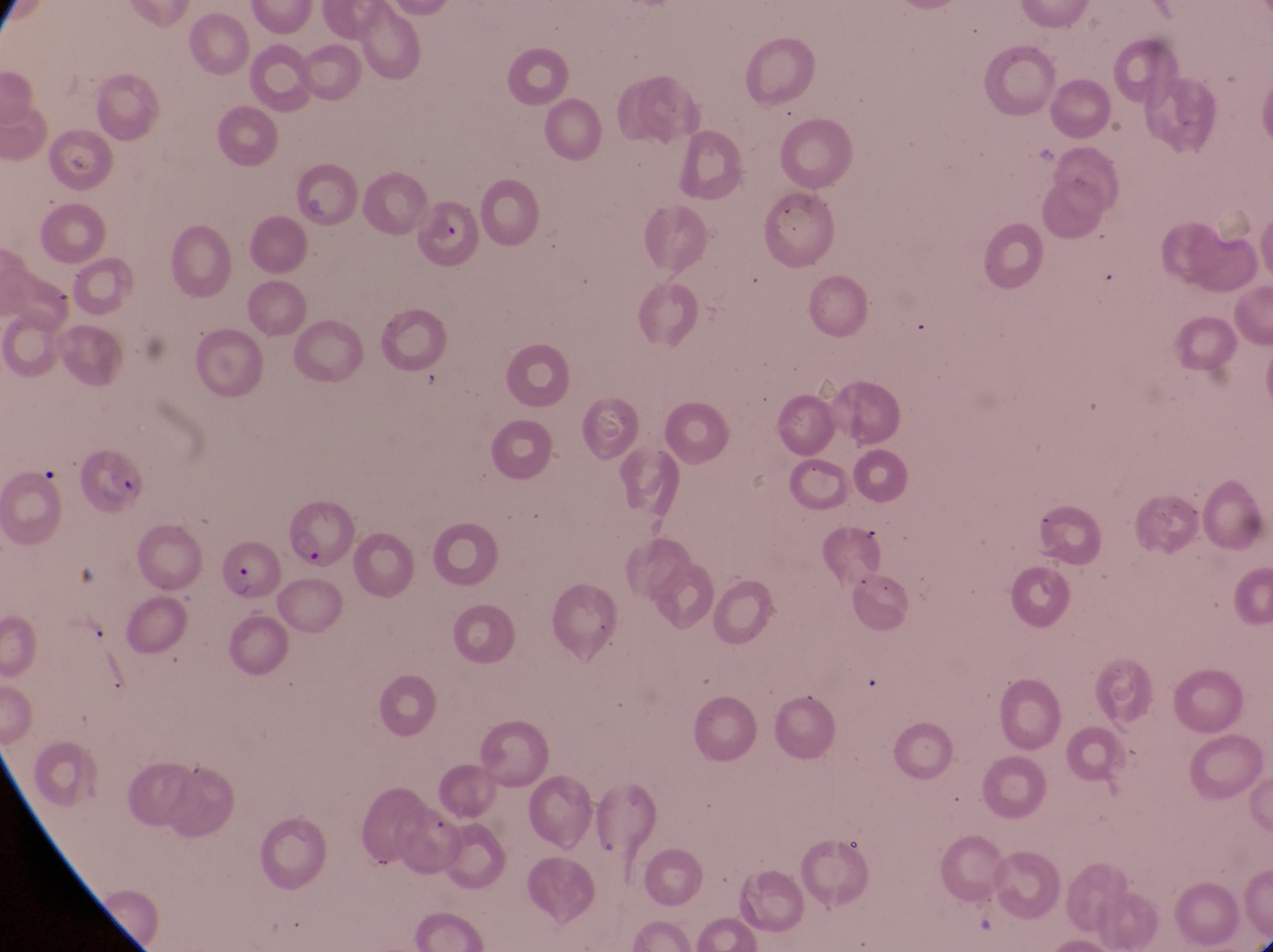
Approximate bounding boxes as left top right bottom in pixels. Parasitised red blood cell locations: 297 165 360 230; 417 193 487 273; 285 495 360 575; 220 544 278 601. Collected in Uganda. Image is 1273×952 pixels. Magnification of 1000x. Single field of view. Thin blood smear. Photographed through the eyepiece of an Olympus CX-23 microscope with a smartphone camera.